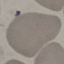 Result: negative for malaria parasites. Cell patch, automatically extracted from a larger field of view and resized to 64 × 64 pixels. Photographed with a smartphone camera at the microscope eyepiece. Thin smear of blood. Giemsa-stained preparation.